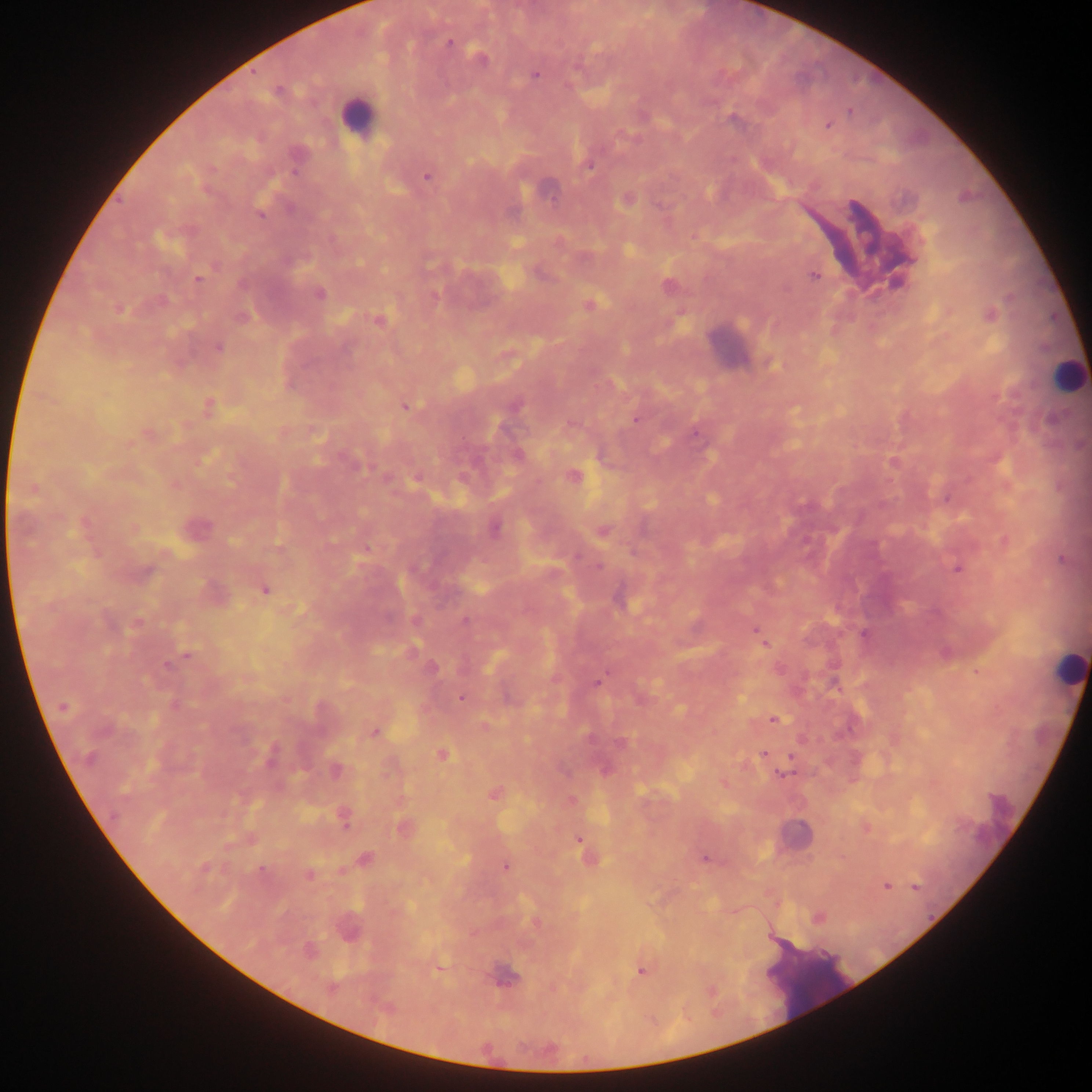
Approximate centers as x y in pixels. Malaria parasite locations: 449 43; 480 57; 535 75; 278 90; 849 111; 827 126; 589 166; 427 177; 627 200; 260 215; 814 275; 900 276; 198 279; 319 293; 589 305; 119 309; 242 317; 378 321; 219 347; 209 406; 406 406; 517 407; 1052 419; 636 420; 571 424; 696 434; 518 454; 893 463; 573 476; 494 529; 603 531; 599 566; 958 568; 265 590; 465 621; 137 623; 759 634; 863 634; 764 643; 188 656; 168 665; 433 668; 597 682; 460 698; 63 707; 773 719; 374 732; 763 754; 442 755; 270 756; 791 758; 336 771; 784 774; 494 794; 344 820; 403 827; 579 840; 366 859; 704 859; 506 867; 204 868; 261 869; 309 875; 886 887; 916 887; 818 918; 348 927; 309 951; 440 969; 641 971; 506 977. Leukocyte locations: 357 117; 548 193; 728 346; 1066 374; 1068 668; 797 834. Image is 1092×1092 pixels. Thick blood film. Mobile-phone photograph taken through the microscope. Sample from Ghana. One field of view.